Assess this cell for malaria.
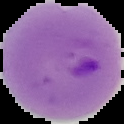
It is parasitized.

preparation = thin blood smear
image size = 124×124 pixels
image type = segmented cell region with the area outside set to black